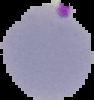

{
  "malaria_status": "parasitized",
  "preparation": "thin blood film",
  "image_size": "94×100 pixels",
  "image_type": "segmented cell region on a black background"
}